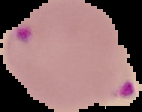

From a thin blood film. Image is 142×112 pixels. Cell region segmented out of the field of view; the surrounding area is masked to black. Malaria status: parasitized.